Outline each uninfected red blood cell.
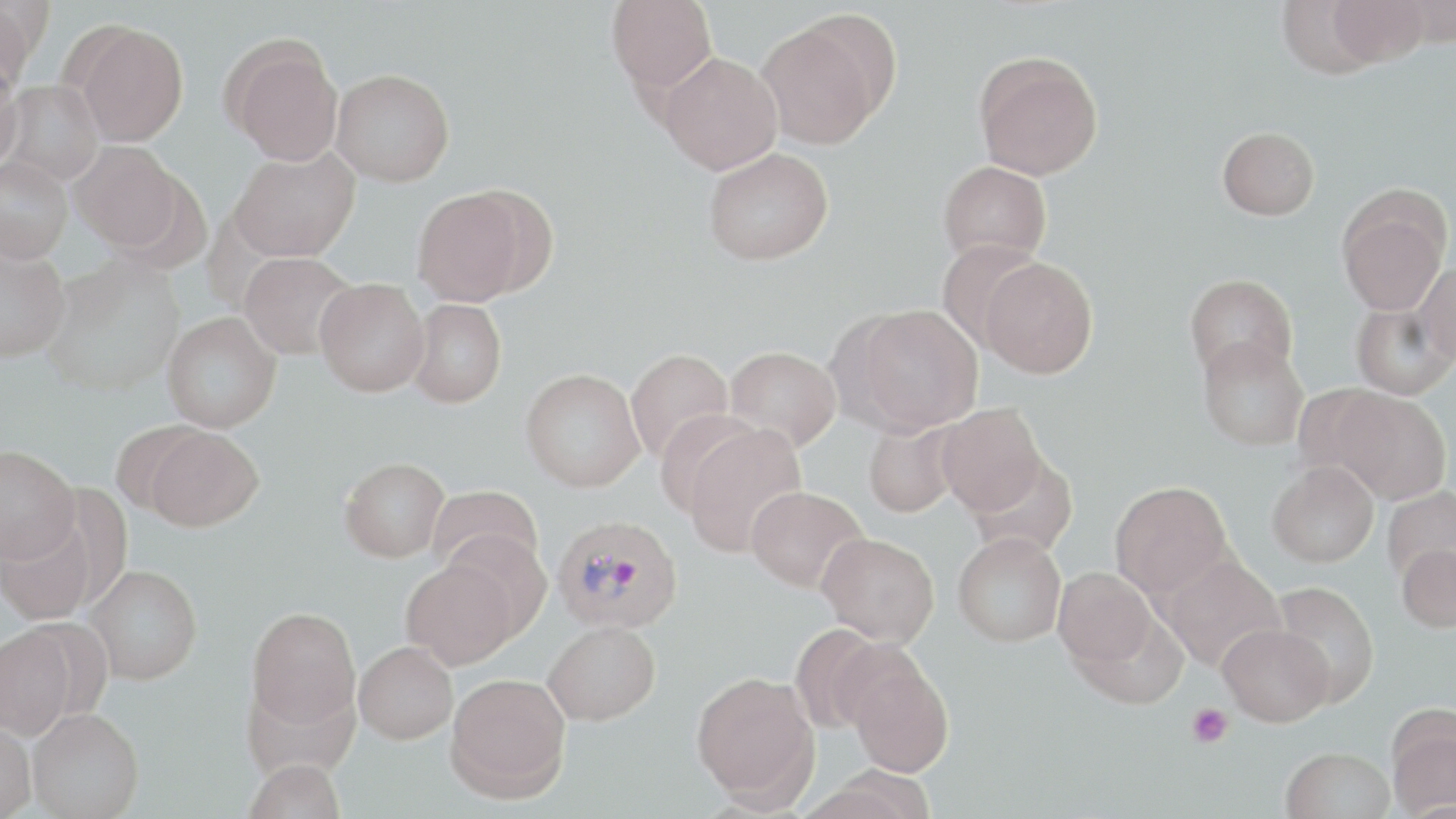

Approximate bounding boxes as [x1, y1, x2, y2] in pixels.
Uninfected red blood cells: [1, 0, 38, 93], [606, 0, 718, 94], [1275, 0, 1386, 79], [1397, 0, 1456, 46], [1329, 1, 1429, 67], [756, 18, 889, 148], [73, 22, 189, 146], [223, 38, 344, 165], [659, 52, 783, 174], [974, 52, 1103, 180], [0, 58, 23, 174], [331, 68, 455, 186], [3, 80, 104, 186], [1217, 126, 1320, 220], [70, 142, 184, 251], [702, 147, 834, 265], [228, 149, 359, 262], [0, 156, 73, 263], [938, 161, 1051, 266], [412, 187, 533, 306], [1338, 200, 1449, 316], [935, 240, 1048, 348], [0, 242, 71, 362], [239, 252, 357, 360], [980, 257, 1098, 378], [42, 258, 184, 396], [1415, 262, 1456, 365], [1184, 273, 1297, 380], [315, 278, 430, 397], [406, 298, 506, 407], [1351, 300, 1456, 399], [847, 304, 983, 435], [162, 312, 281, 432], [1198, 336, 1309, 452], [725, 346, 841, 452], [624, 347, 734, 464], [520, 367, 645, 492], [1330, 388, 1451, 504], [936, 402, 1047, 516], [863, 418, 963, 517], [680, 421, 808, 558], [142, 425, 264, 532], [0, 444, 79, 564], [967, 455, 1079, 558], [340, 456, 449, 562], [1267, 461, 1379, 568], [1110, 480, 1233, 599], [745, 485, 868, 592], [428, 486, 545, 577], [1382, 486, 1456, 587], [0, 510, 99, 626], [441, 529, 553, 639], [953, 532, 1066, 647], [817, 533, 940, 646], [1397, 542, 1456, 632], [1160, 555, 1285, 671], [401, 558, 519, 669], [84, 563, 202, 684], [1053, 566, 1160, 673], [1271, 581, 1380, 706], [246, 606, 360, 728], [543, 620, 661, 725], [0, 623, 76, 740], [1217, 623, 1333, 726], [788, 624, 894, 734], [354, 641, 458, 744], [845, 651, 955, 777], [690, 671, 819, 805], [445, 672, 571, 802], [1386, 707, 1456, 817], [28, 708, 144, 819], [0, 718, 36, 818], [1281, 746, 1394, 818], [243, 758, 347, 819].

Platelet locations: [1186, 703, 1234, 748]. Plasmodium vivax-infected red blood cell locations: [552, 514, 684, 635]. Slide-level diagnosis: Plasmodium vivax. Image is 1456×819 pixels. 1000x magnification. Optical microscopy. May-Grünwald-Giemsa stain. Thin blood film. Single field of view.